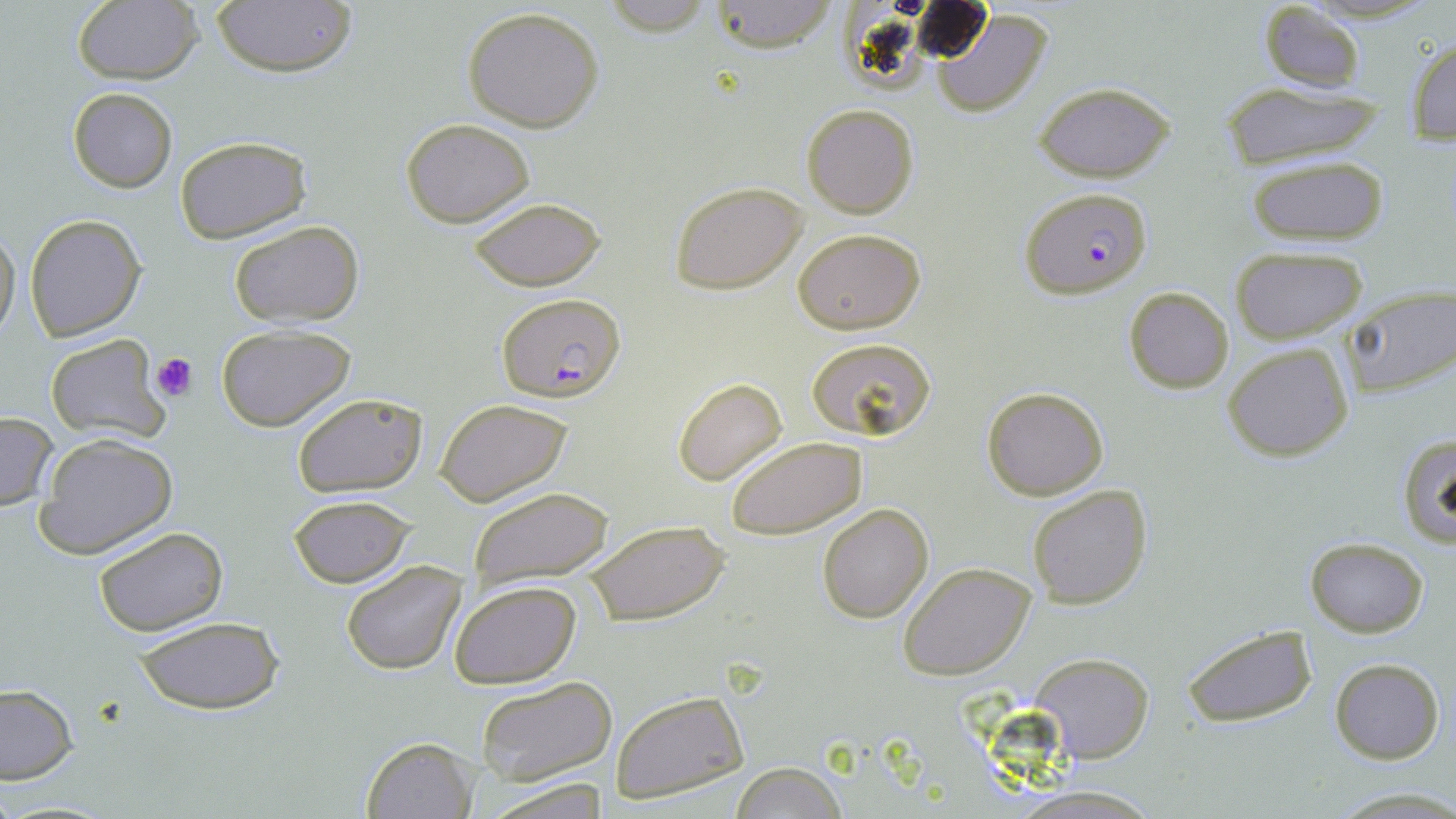
slide-level diagnosis = Plasmodium falciparum
preparation = thin blood smear
field of view = single
image size = 1456×819 pixels
Plasmodium falciparum-infected red blood cell locations = approximate bounding boxes as [x1, y1, x2, y2] in pixels: [1020, 188, 1153, 297], [495, 291, 627, 402]
modality = light microscopy
platelet locations = approximate bounding boxes as [x1, y1, x2, y2] in pixels: [152, 352, 198, 401]
stain = May-Grünwald-Giemsa
uninfected red blood cell locations = approximate bounding boxes as [x1, y1, x2, y2] in pixels: [71, 0, 203, 84], [599, 0, 715, 36], [705, 0, 840, 52], [211, 1, 358, 79], [1255, 3, 1367, 94], [462, 7, 606, 133], [930, 9, 1054, 116], [1406, 36, 1456, 145], [1214, 80, 1392, 170], [1033, 81, 1177, 181], [68, 88, 176, 193], [801, 103, 919, 219], [401, 117, 535, 227], [174, 134, 312, 242], [1246, 156, 1389, 247], [670, 180, 808, 295], [467, 197, 607, 290], [24, 214, 146, 340], [228, 219, 366, 328], [0, 226, 19, 339], [793, 227, 925, 335], [1230, 247, 1368, 343], [1341, 285, 1456, 398], [1124, 286, 1233, 393], [215, 322, 356, 431], [44, 333, 166, 443], [805, 335, 938, 441], [1223, 343, 1353, 462], [673, 378, 788, 485], [981, 385, 1109, 499], [291, 392, 426, 496], [435, 396, 574, 507], [0, 412, 58, 510], [1396, 432, 1456, 546], [724, 434, 868, 538], [36, 435, 177, 559], [1026, 485, 1152, 610], [466, 487, 613, 590], [288, 495, 414, 587], [817, 503, 933, 623], [583, 519, 729, 627], [94, 528, 227, 636], [1306, 536, 1429, 636], [342, 560, 467, 675], [899, 563, 1037, 680], [448, 579, 583, 689], [132, 616, 283, 714], [1181, 624, 1320, 729], [1029, 650, 1153, 764], [1329, 658, 1445, 765], [474, 676, 619, 788], [0, 685, 77, 783], [609, 688, 748, 803], [361, 734, 477, 818], [728, 762, 852, 818], [482, 778, 609, 818]
magnification = 1000x